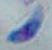

magnification: 1000x
modality: photomicrograph
identification: Toxoplasma gondii